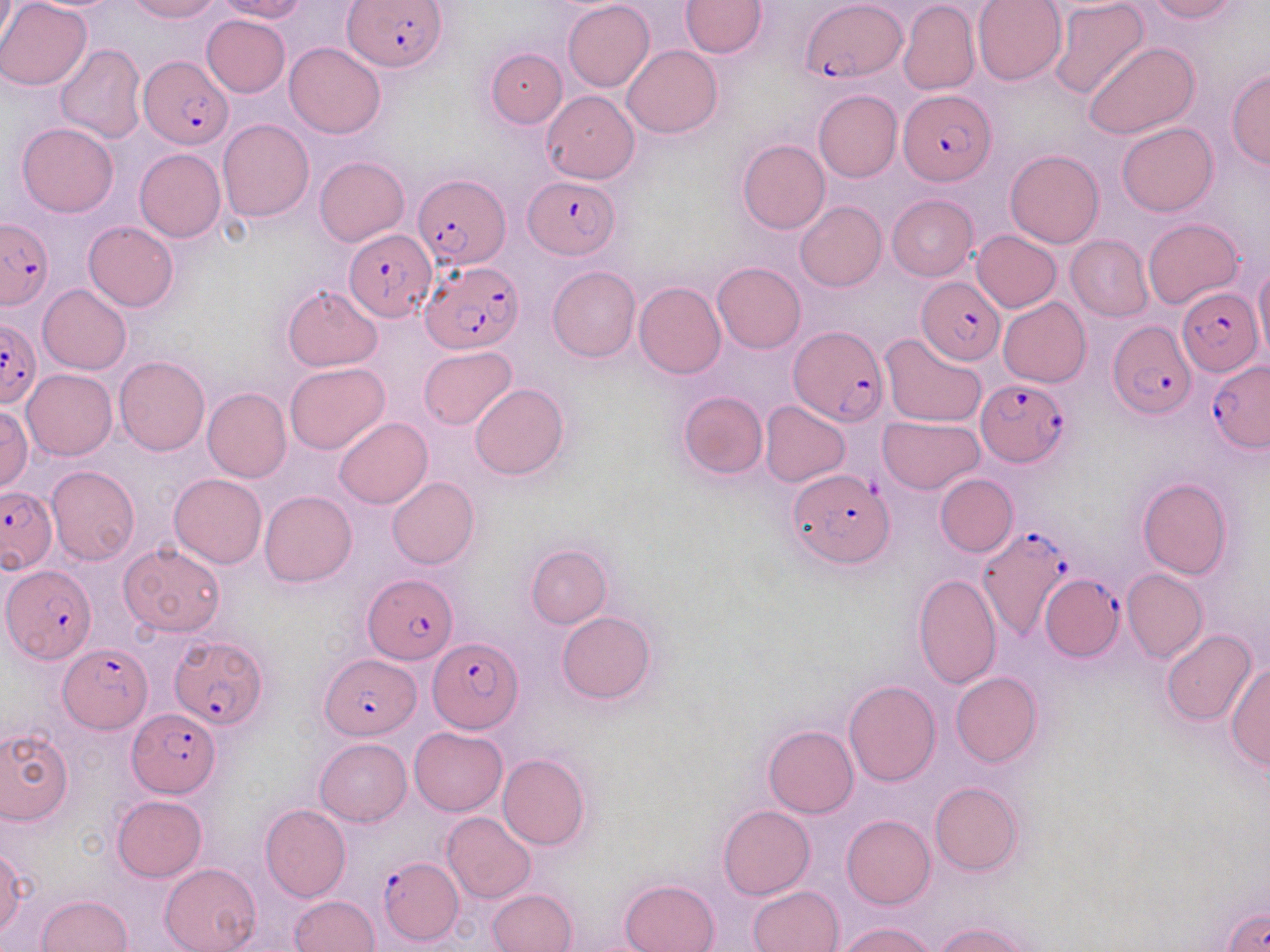
Approximate bounding boxes as (x1, y1, x2, y2) in pixels. Uninfected red blood cell locations: (0, 0, 91, 90), (0, 0, 16, 50), (127, 0, 220, 22), (214, 0, 310, 22), (563, 0, 654, 90), (974, 0, 1066, 85), (1146, 0, 1239, 22), (680, 1, 766, 57), (1049, 1, 1149, 100), (899, 2, 979, 95), (201, 14, 290, 98), (1084, 41, 1199, 140), (285, 42, 387, 138), (56, 43, 147, 142), (622, 46, 723, 138), (486, 48, 567, 127), (1227, 70, 1270, 169), (814, 89, 902, 183), (541, 90, 639, 184), (218, 119, 314, 222), (1117, 121, 1218, 216), (17, 123, 118, 217), (737, 139, 829, 235), (134, 148, 226, 242), (1005, 149, 1104, 248), (315, 156, 408, 246), (887, 194, 977, 281), (795, 201, 887, 292), (1143, 219, 1244, 309), (84, 221, 178, 311), (972, 231, 1061, 311), (1066, 235, 1154, 321), (712, 262, 805, 353), (1254, 263, 1270, 362), (547, 266, 640, 362), (635, 282, 726, 378), (38, 284, 131, 375), (282, 284, 381, 370), (998, 296, 1090, 388), (880, 333, 987, 427), (418, 345, 516, 431), (114, 357, 210, 456), (285, 362, 390, 454), (23, 369, 116, 461), (469, 383, 569, 480), (202, 387, 291, 482), (678, 391, 767, 480), (760, 401, 850, 486), (0, 406, 32, 491), (877, 416, 984, 494), (335, 418, 432, 508), (46, 466, 139, 565), (169, 473, 267, 568), (934, 473, 1018, 557), (387, 475, 478, 569), (1137, 477, 1232, 579), (259, 490, 356, 587), (120, 543, 226, 637), (526, 543, 611, 629), (1121, 569, 1206, 663), (913, 572, 1001, 688), (557, 612, 655, 703), (1162, 630, 1256, 727), (1228, 662, 1269, 771), (951, 672, 1042, 767), (844, 681, 940, 786), (763, 725, 858, 818), (409, 726, 507, 815), (0, 727, 72, 825), (315, 737, 412, 826), (498, 753, 590, 851), (931, 782, 1023, 877), (112, 795, 206, 881), (260, 804, 351, 902), (718, 805, 814, 900), (443, 813, 536, 902), (842, 813, 935, 909), (1, 849, 27, 938), (160, 863, 261, 952), (620, 878, 719, 952), (747, 886, 842, 952), (487, 889, 577, 952), (37, 894, 133, 951), (289, 896, 378, 952), (838, 920, 938, 952), (935, 920, 1035, 951). Plasmodium falciparum-infected red blood cell locations: (347, 1, 447, 73), (802, 2, 907, 82), (139, 55, 235, 148), (898, 89, 994, 184), (412, 172, 509, 271), (525, 176, 618, 259), (0, 218, 54, 308), (344, 230, 435, 321), (422, 260, 522, 354), (916, 278, 1005, 365), (1176, 288, 1263, 376), (1106, 318, 1194, 418), (0, 319, 41, 408), (790, 327, 888, 425), (1208, 359, 1270, 451), (977, 377, 1071, 468), (786, 468, 895, 569), (0, 485, 57, 572), (976, 523, 1070, 642), (2, 562, 95, 662), (1042, 572, 1124, 661), (363, 575, 459, 664), (167, 632, 269, 734), (429, 637, 524, 733), (60, 643, 150, 733), (322, 654, 420, 738), (129, 708, 218, 796), (380, 856, 462, 944). Slide-level diagnosis: Plasmodium falciparum. Light microscopy. Image is 1270×952 pixels. May-Grünwald-Giemsa-stained preparation. Captured at 1000x magnification. Single field of view. Thin blood smear.